Assess this cell for malaria.
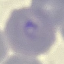

It is parasitized.

{
  "preparation": "thin blood film",
  "capture": "smartphone camera at the microscope eyepiece",
  "stain": "Giemsa",
  "image_type": "cell patch, automatically extracted from a larger field of view and resized to 64 × 64 pixels"
}